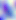

modality = micrograph
magnification = 400x
identification = Toxoplasma gondii